Report the malaria status of this cell.
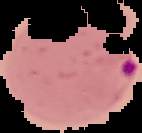

It is parasitized.

From a thin blood smear. Image is 142×133 pixels. Segmented cell region on a black background.